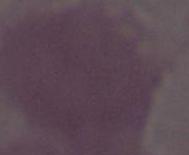

{
  "identification": "red blood cell",
  "magnification": "1000x",
  "modality": "photomicrograph"
}